Assess the morphology of the red blood cells.
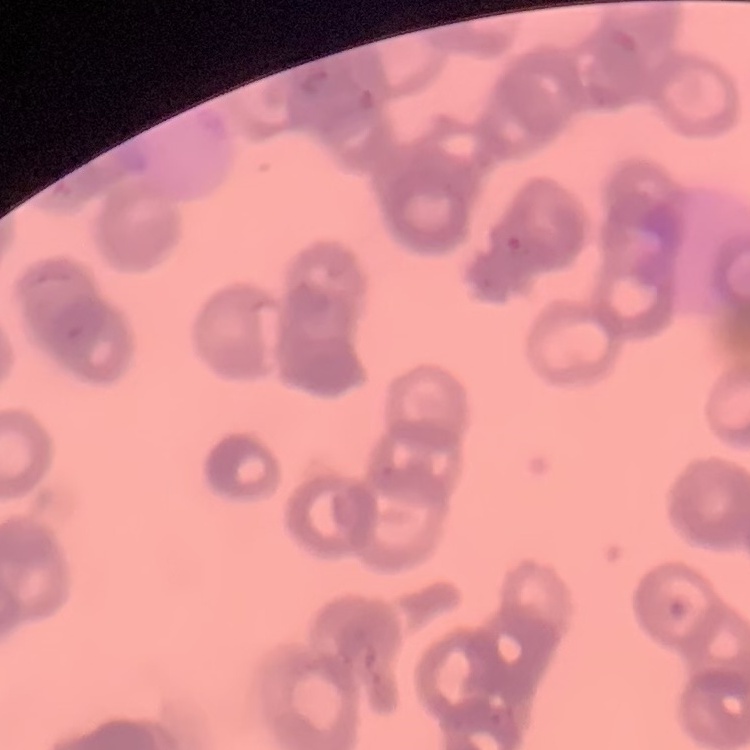
Rouleaux formation.

Thin blood film. Field's or Giemsa stain. Square crop of a larger photomicrograph.